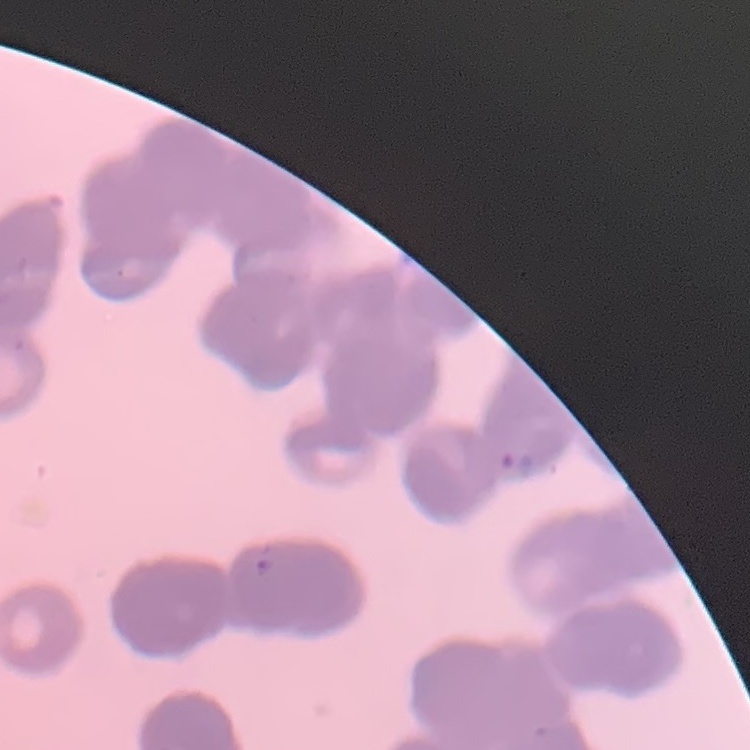
The erythrocytes show rouleaux formation. Square crop of a larger photomicrograph. Stained with either Field's or Giemsa. Thin peripheral smear.